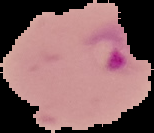 Result: Plasmodium parasites detected. From a thin blood film. Cell region segmented out of the field of view; the surrounding area is masked to black. Image is 154×133 pixels.